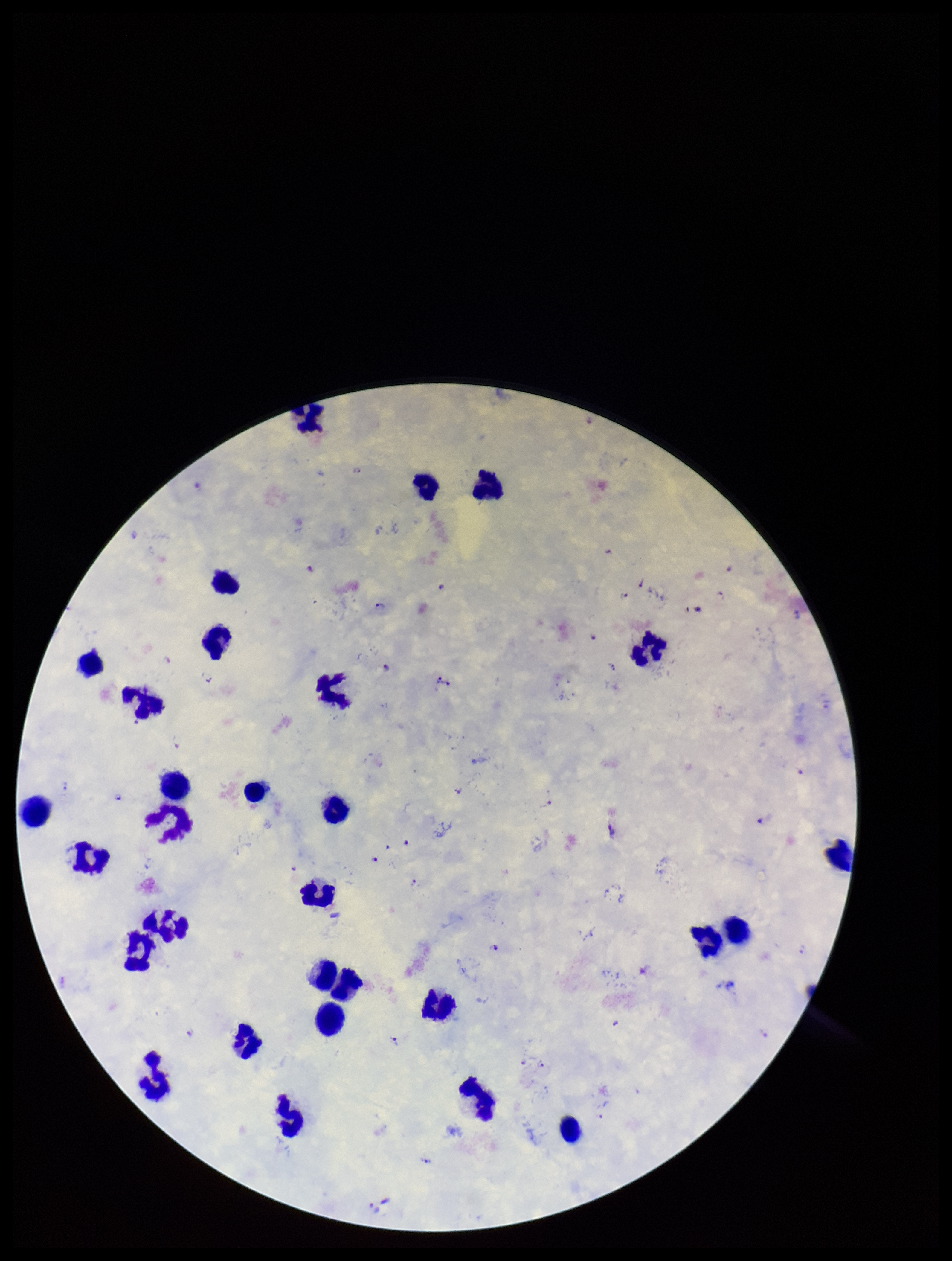
{
  "parasite_count": 28,
  "plasmodium_parasites": "identified",
  "preparation": "thick",
  "stain": "Giemsa",
  "field_of_view": "one from this slide",
  "leukocyte_count": 32,
  "species_reported_for_this_patient": "Plasmodium falciparum",
  "capture": "smartphone photograph through the microscope eyepiece",
  "patient_malaria_status": "positive",
  "image_size": "952×1261 pixels"
}